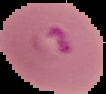
Summary:
  - Result: Plasmodium parasites identified
  - Image type: segmented cell region on a black background
  - Image size: 106×94 pixels
  - Preparation: thin blood smear